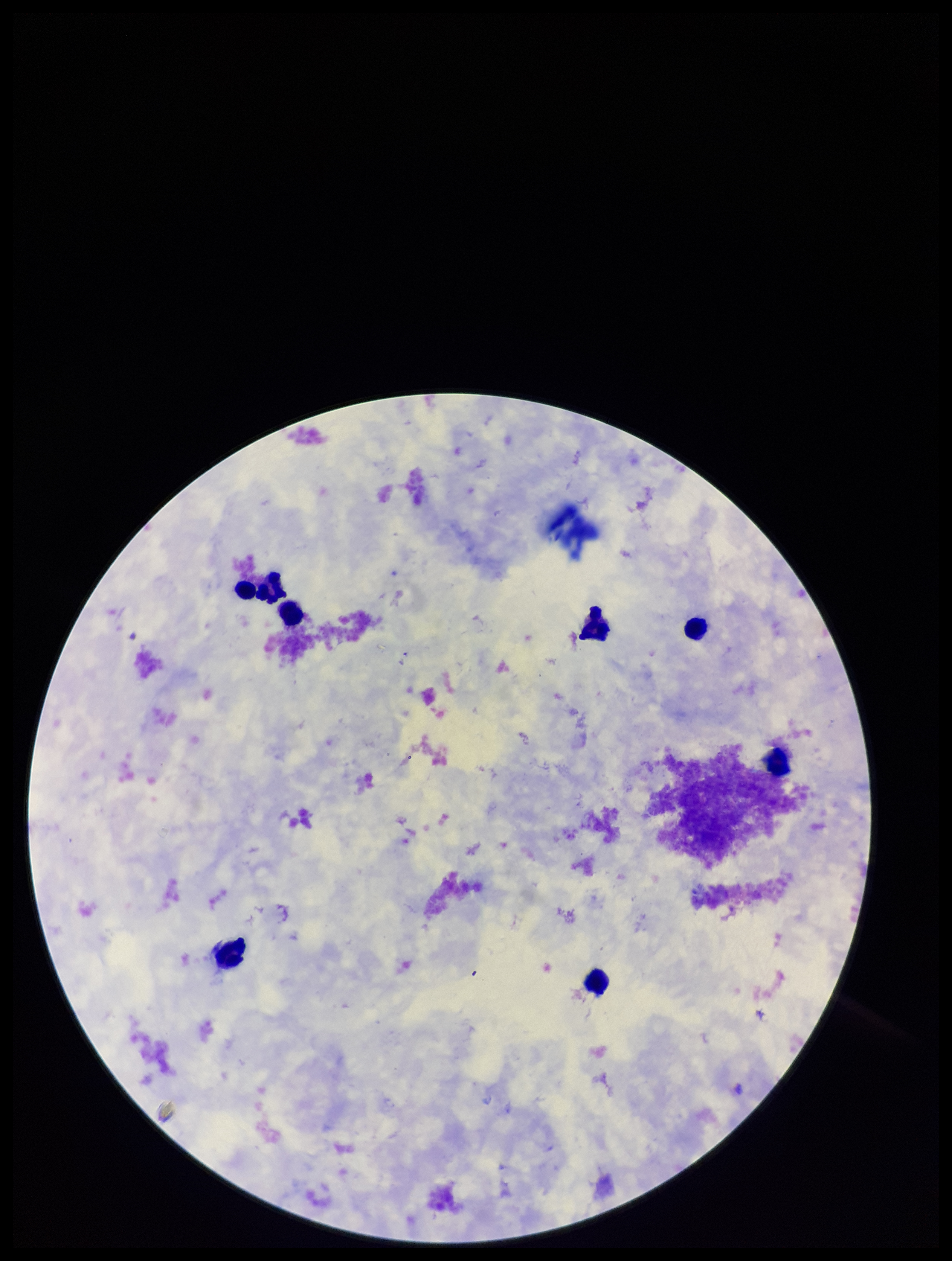
Image is 952×1261 pixels. Giemsa stain. Patient malaria status: negative. Leukocyte count: 7. Single field of view. Preparation: thick smear. Plasmodium parasites: none identified. Smartphone photograph taken through the eyepiece of a microscope. Parasite count: 0.